Describe the morphology of the red blood cells.
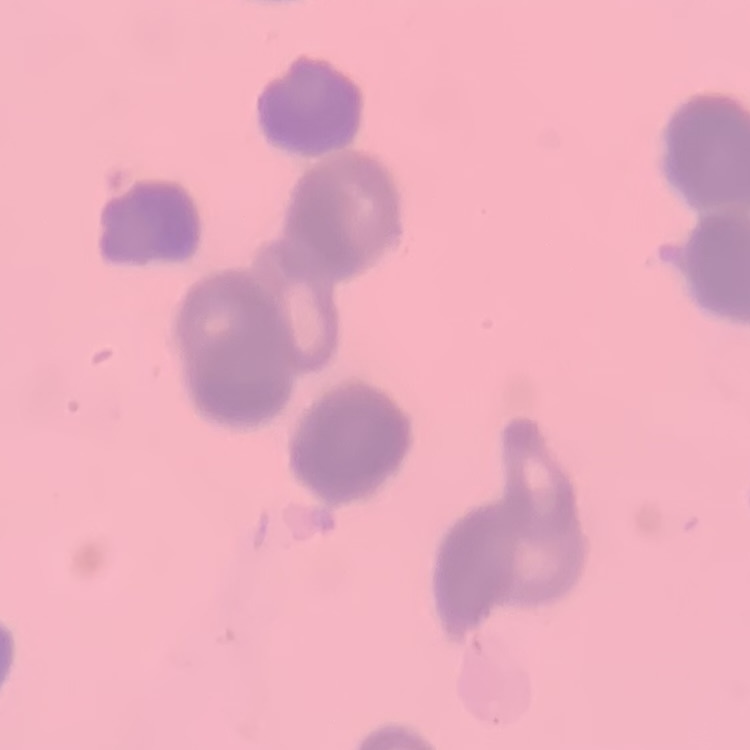
They show rouleaux formation.

Square crop of a larger photomicrograph. Thin peripheral smear. Stained with either Field's or Giemsa.